Describe the morphology of the erythrocytes.
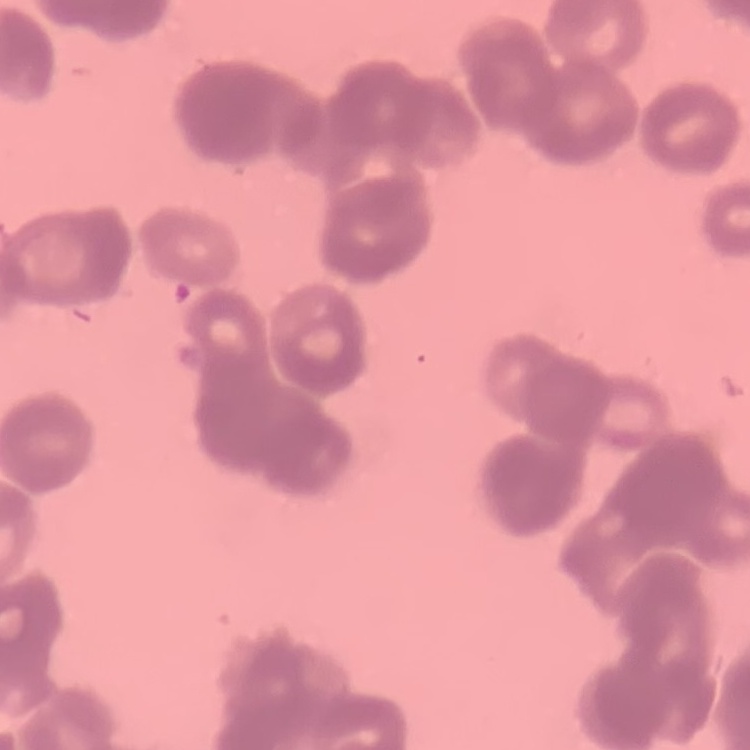

Rouleaux formation.

stain = Field's or Giemsa
preparation = thin blood film
image type = square crop of a larger photomicrograph